Describe the morphology of the red blood cells.
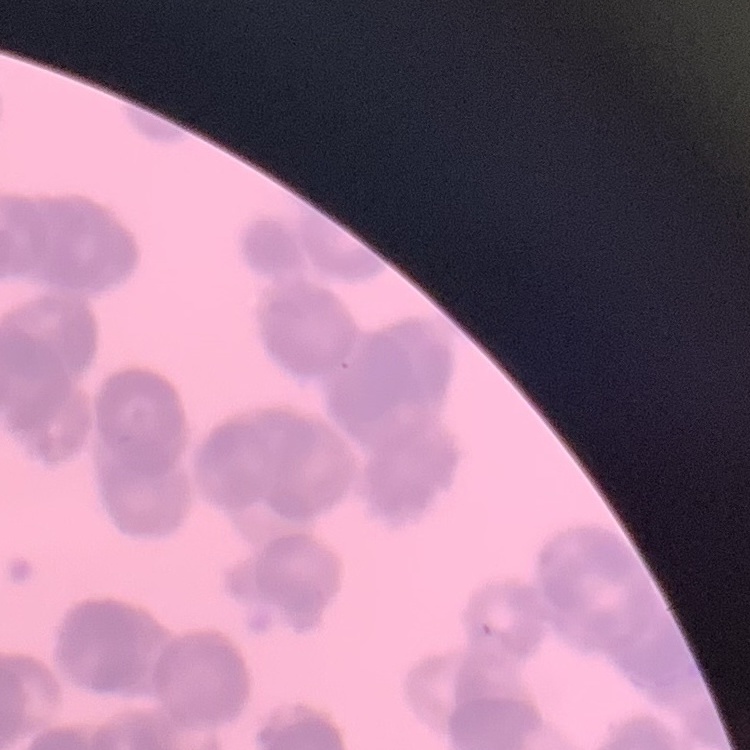
They show rouleaux formation.

Summary:
  - Preparation: thin peripheral smear
  - Image type: square crop of a larger photomicrograph
  - Stain: Field's or Giemsa